Outline platelets.
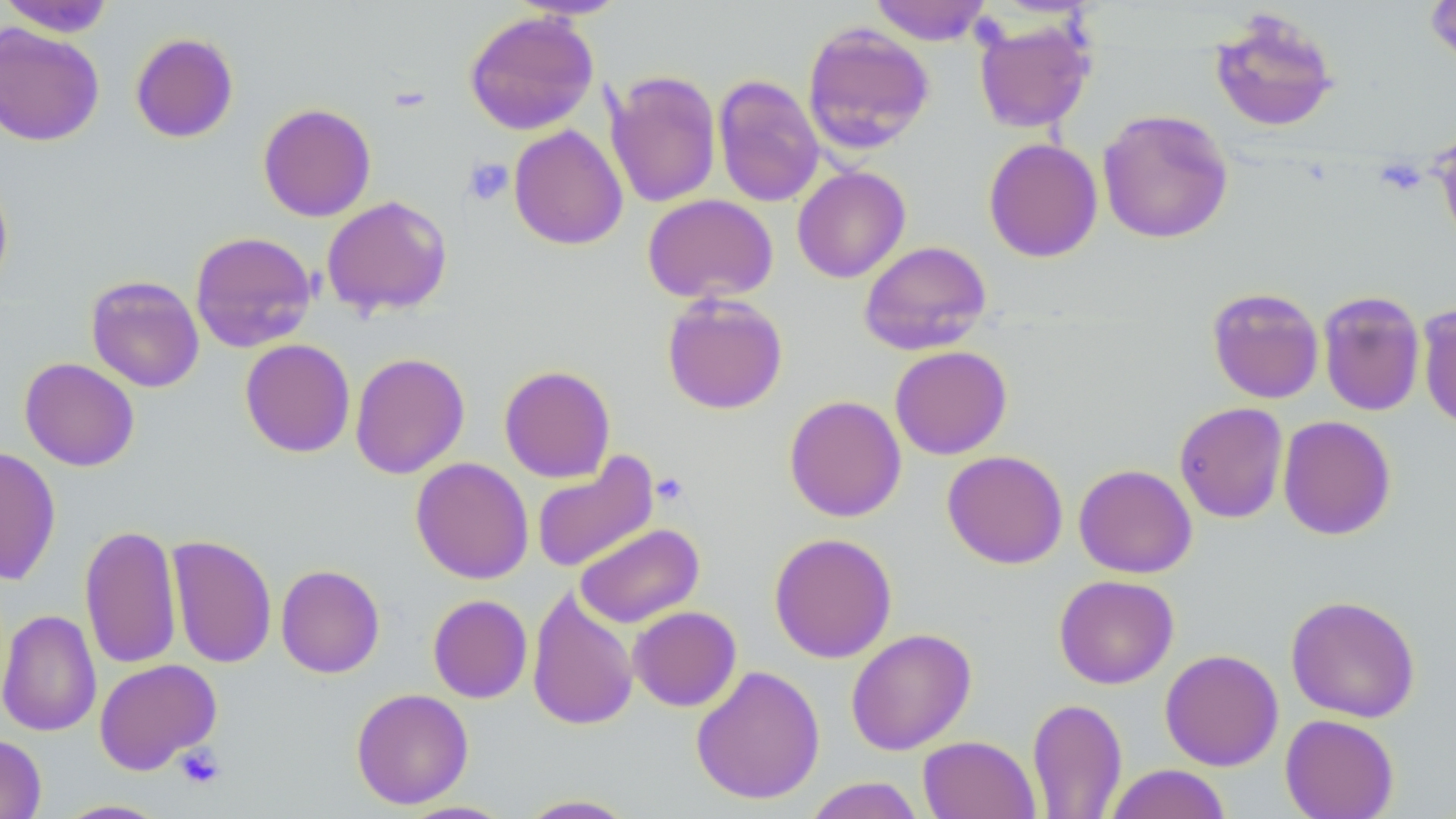

Approximate bounding boxes as (x1,y1)-(x2,y2) corner pairs in pixels.
Platelets: (463,158)-(514,206), (651,472)-(690,506), (174,745)-(225,789).

slide_level_diagnosis: negative for blood parasites
image_size: 1456×819 pixels
field_of_view: single
stain: May-Grünwald-Giemsa
preparation: thin blood smear
modality: optical microscopy
uninfected_red_blood_cell_locations: 'approximate bounding boxes as (x1,y1)-(x2,y2) corner pairs in pixels: (0,0)-(116,38), (505,0)-(630,20), (869,0)-(992,45), (1422,0)-(1456,70), (1208,8)-(1341,134), (464,10)-(599,135), (972,17)-(1097,133), (801,22)-(935,155), (0,23)-(104,147), (130,32)-(239,143), (605,69)-(722,209), (713,74)-(825,208), (258,103)-(376,222), (1097,108)-(1234,244), (508,124)-(628,251), (1435,130)-(1456,251), (983,138)-(1103,263), (792,166)-(910,283), (0,170)-(14,296), (642,194)-(778,304), (321,195)-(453,317), (189,231)-(318,353), (858,240)-(992,355), (86,275)-(204,393), (1207,287)-(1324,404), (1317,289)-(1426,417), (662,293)-(788,415), (1417,303)-(1456,430), (239,338)-(356,458), (889,345)-(1012,460), (349,352)-(470,480), (19,357)-(139,471), (498,364)-(616,483), (784,395)-(906,522), (1174,402)-(1289,524), (1278,415)-(1396,540), (0,446)-(61,586), (942,450)-(1068,569), (531,453)-(658,573), (411,457)-(534,584), (1073,464)-(1197,578), (79,523)-(182,670), (575,523)-(704,628), (769,532)-(897,663), (166,535)-(277,669), (276,564)-(384,678), (1054,574)-(1179,689), (527,587)-(639,732), (427,594)-(533,703), (1285,594)-(1421,723), (628,606)-(742,711), (0,608)-(101,737), (846,628)-(976,755), (1160,649)-(1284,771), (94,658)-(221,775), (690,664)-(825,805), (351,687)-(474,809), (1026,697)-(1128,818), (1280,714)-(1400,819), (0,733)-(46,819), (918,735)-(1040,819), (1104,764)-(1232,819), (801,776)-(927,819), (515,794)-(640,818), (54,799)-(172,818), (397,800)-(516,818)'
magnification: 1000x